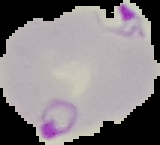 From a thin blood film. Malaria status: parasitized. Segmented cell region on a black background. Image is 160×145 pixels.